Describe the morphology of the erythrocytes.
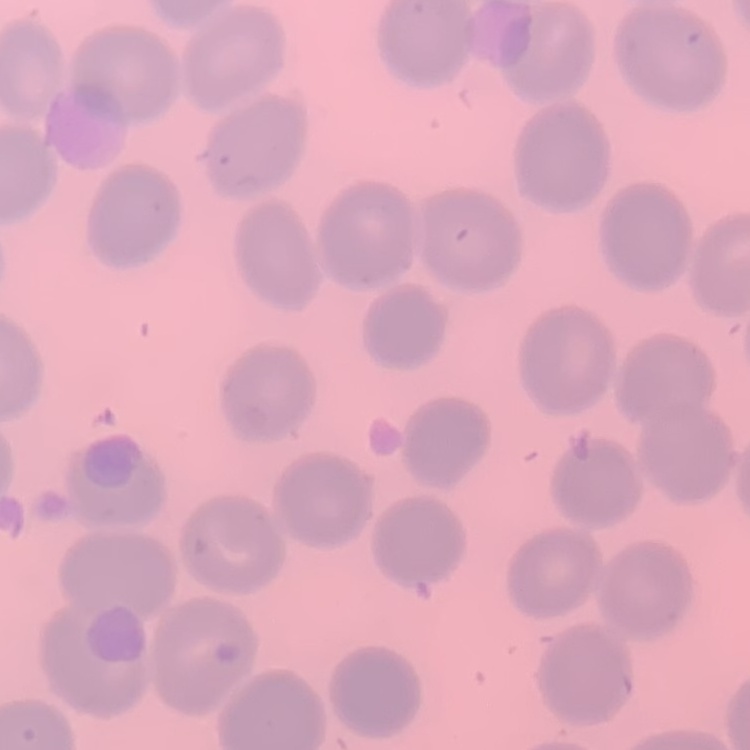

They show no rouleaux formation.

Square crop of a larger photomicrograph. Thin peripheral smear. Stained with either Field's or Giemsa.